Identify the cell.
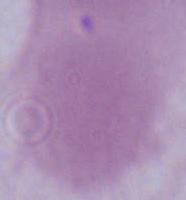

This is an erythrocyte.

Summary:
  - Modality: micrograph
  - Magnification: 1000x